Identify the blood parasite species.
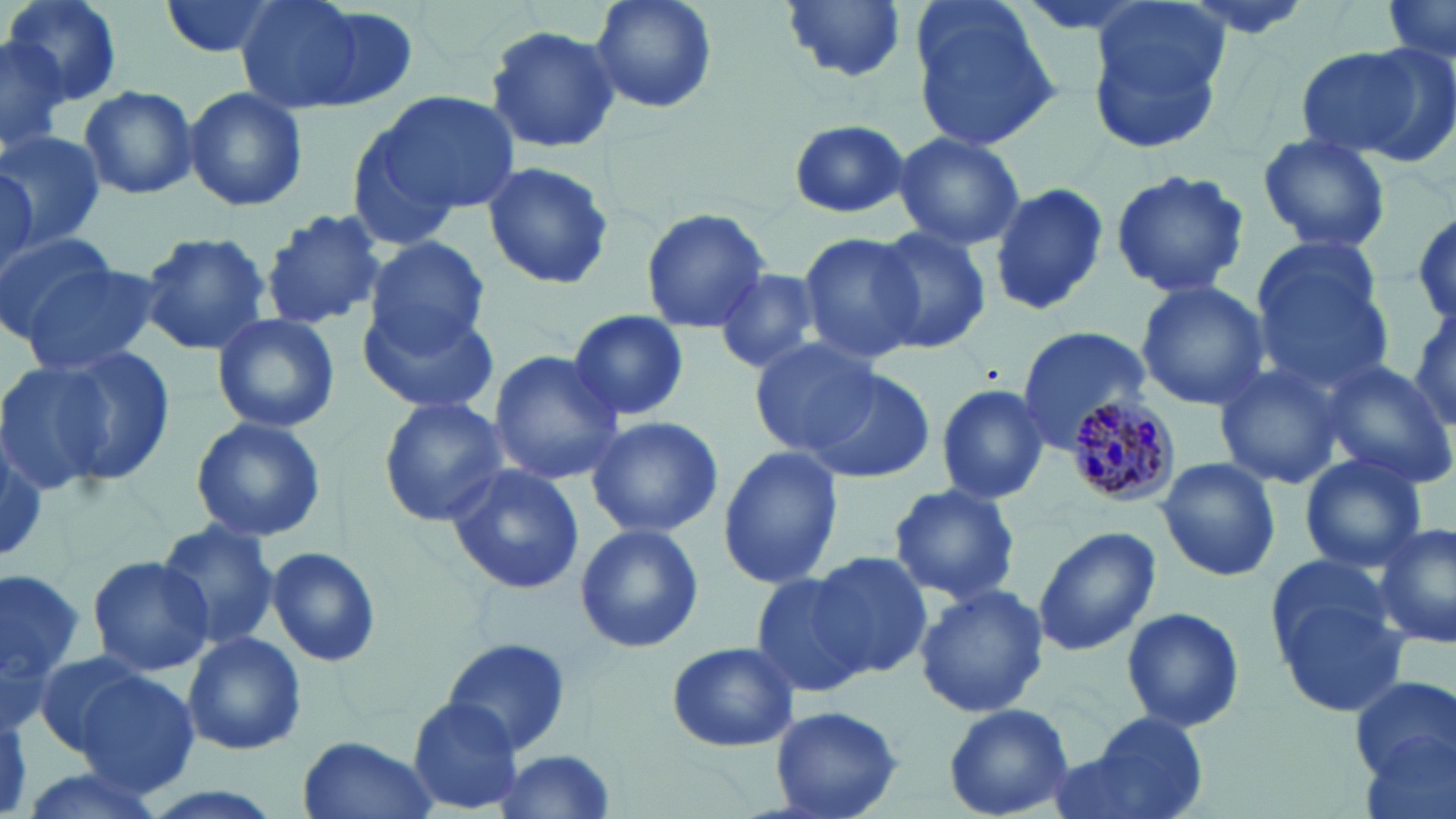
Plasmodium malariae.

field of view = one of a larger specimen
preparation = thin blood film
modality = optical microscopy
image size = 1456×819 pixels
magnification = 1000x
Plasmodium malariae-infected red blood cell locations = approximate bounding boxes as (x1,y1)-(x2,y2) corner pairs in pixels: (1065,393)-(1179,508)
stain = May-Grünwald-Giemsa
uninfected red blood cell locations = approximate bounding boxes as (x1,y1)-(x2,y2) corner pairs in pixels: (8,0)-(122,104), (156,0)-(289,60), (234,0)-(402,117), (589,0)-(717,115), (780,0)-(907,83), (1381,0)-(1454,64), (909,3)-(1062,151), (1085,6)-(1229,150), (485,24)-(622,154), (0,37)-(68,155), (1296,43)-(1448,165), (78,84)-(197,200), (183,87)-(308,212), (373,89)-(518,216), (344,118)-(475,250), (786,121)-(914,218), (0,131)-(105,248), (891,131)-(1026,251), (1256,135)-(1391,253), (478,160)-(616,291), (0,163)-(37,278), (1108,167)-(1250,300), (988,183)-(1108,318), (640,206)-(772,334), (260,208)-(387,329), (1410,209)-(1456,330), (870,226)-(991,354), (0,229)-(119,341), (139,230)-(272,356), (798,232)-(923,362), (367,235)-(489,351), (1248,244)-(1391,388), (16,259)-(161,377), (713,266)-(829,376), (1136,281)-(1269,409), (357,302)-(502,415), (568,309)-(689,423), (1407,309)-(1456,431), (213,314)-(339,433), (1015,325)-(1148,450), (749,339)-(883,457), (6,350)-(165,489), (486,351)-(625,483), (1315,359)-(1456,490), (1212,361)-(1347,489), (806,367)-(935,485), (933,383)-(1051,504), (378,398)-(513,525), (583,415)-(726,538), (189,416)-(327,543), (1,444)-(50,558), (717,447)-(843,587), (1298,453)-(1428,572), (1157,459)-(1281,580), (445,460)-(587,594), (887,483)-(1022,606), (155,519)-(282,651), (1374,522)-(1456,651), (574,523)-(703,652), (1032,527)-(1161,655), (266,545)-(382,668), (813,550)-(935,679), (88,555)-(213,678), (0,565)-(84,715), (1269,568)-(1410,715), (749,570)-(870,698), (913,583)-(1049,719), (1122,605)-(1245,733), (182,632)-(306,755), (442,637)-(574,753), (665,641)-(799,753), (29,651)-(157,757), (74,671)-(200,800), (1349,675)-(1455,787), (407,698)-(524,812), (943,703)-(1076,818), (765,706)-(906,819), (1078,711)-(1211,819), (297,735)-(437,819), (489,752)-(621,818), (13,765)-(169,819), (131,782)-(291,819)